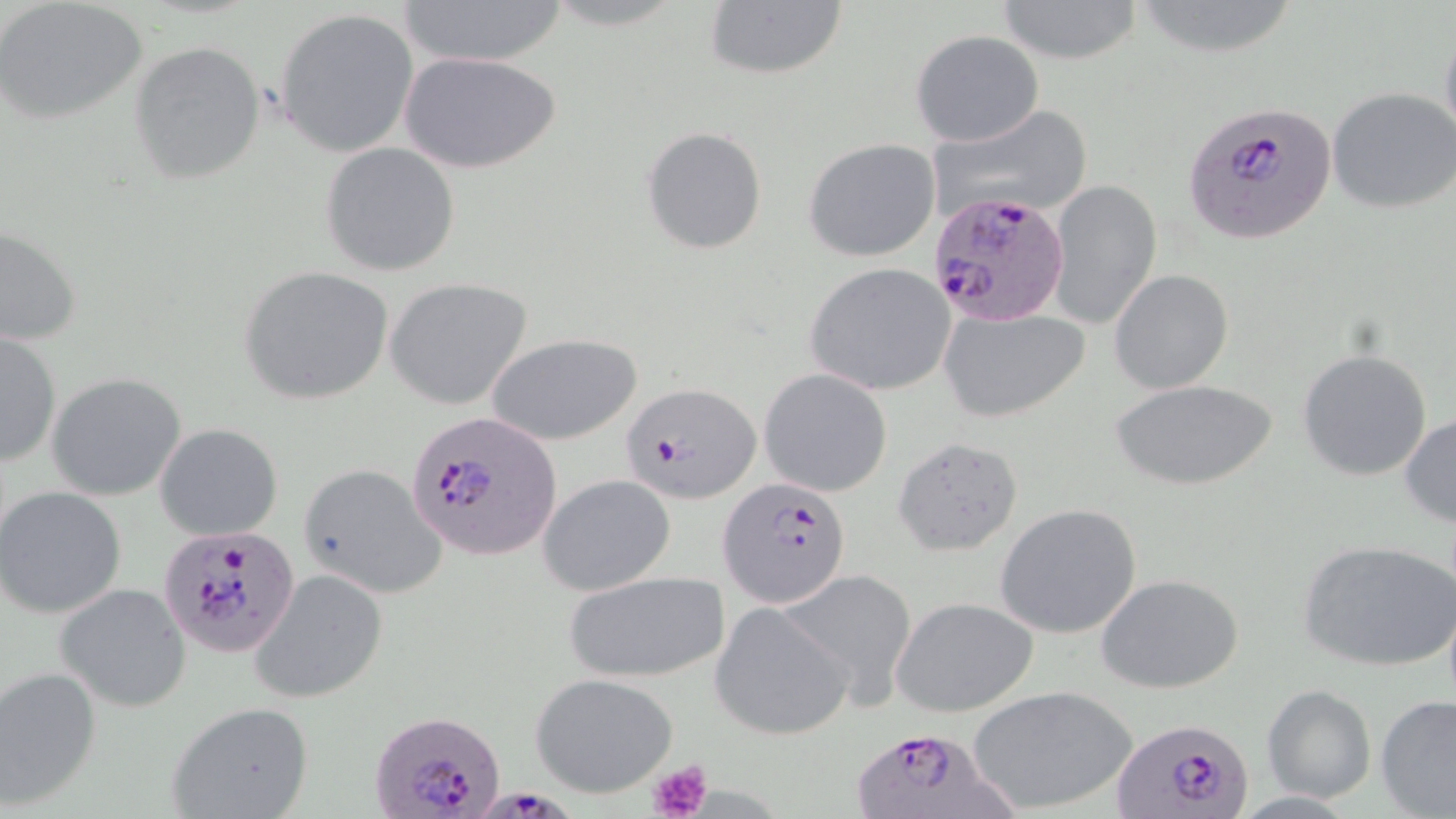

Summary:
  - Coordinate format: approximate bounding boxes as (x1, y1, x2, y2) in pixels
  - Uninfected red blood cell locations: (404, 0, 564, 68), (995, 0, 1144, 66), (0, 1, 149, 123), (702, 1, 847, 81), (1132, 1, 1294, 61), (275, 7, 419, 159), (1438, 23, 1456, 153), (911, 29, 1043, 146), (130, 41, 267, 184), (401, 51, 561, 174), (1327, 86, 1456, 213), (927, 104, 1092, 221), (641, 125, 769, 255), (804, 138, 942, 263), (320, 142, 461, 276), (1046, 180, 1160, 331), (2, 225, 81, 347), (806, 261, 958, 397), (240, 266, 395, 404), (1109, 270, 1233, 393), (384, 278, 534, 411), (939, 306, 1090, 423), (0, 331, 61, 466), (486, 332, 642, 446), (1299, 348, 1433, 481), (760, 369, 892, 496), (47, 373, 186, 500), (1112, 379, 1276, 492), (1400, 413, 1456, 526), (156, 422, 283, 540), (892, 435, 1024, 556), (299, 464, 447, 599), (539, 474, 675, 596), (0, 486, 127, 617), (994, 502, 1142, 638), (1297, 540, 1454, 671), (779, 568, 919, 706), (250, 569, 387, 704), (562, 570, 729, 683), (1098, 572, 1245, 693), (55, 584, 191, 711), (891, 597, 1039, 718), (710, 601, 852, 741), (0, 667, 102, 808), (530, 672, 679, 799), (1262, 684, 1376, 802), (967, 685, 1139, 816), (1376, 694, 1456, 819), (167, 700, 315, 819)
  - Plasmodium falciparum-infected red blood cell locations: (1185, 101, 1337, 247), (932, 190, 1071, 325), (620, 380, 761, 504), (403, 409, 564, 566), (721, 477, 850, 608), (159, 525, 299, 656), (370, 707, 505, 818), (1111, 716, 1253, 819), (848, 725, 1015, 819), (471, 779, 586, 819)
  - Platelet locations: (644, 757, 714, 819)
  - Slide-level diagnosis: Plasmodium falciparum
  - Magnification: 1000x
  - Stain: May-Grünwald-Giemsa
  - Preparation: thin blood smear
  - Modality: optical microscopy
  - Image size: 1456×819 pixels
  - Field of view: one of a larger specimen